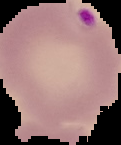
Malaria status: parasitized. From a thin blood smear. The area outside the segmented cell region is set to black. Image is 121×145 pixels.